Identify the cell.
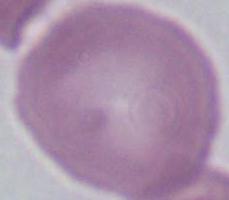
An erythrocyte.

magnification = 1000x
modality = micrograph